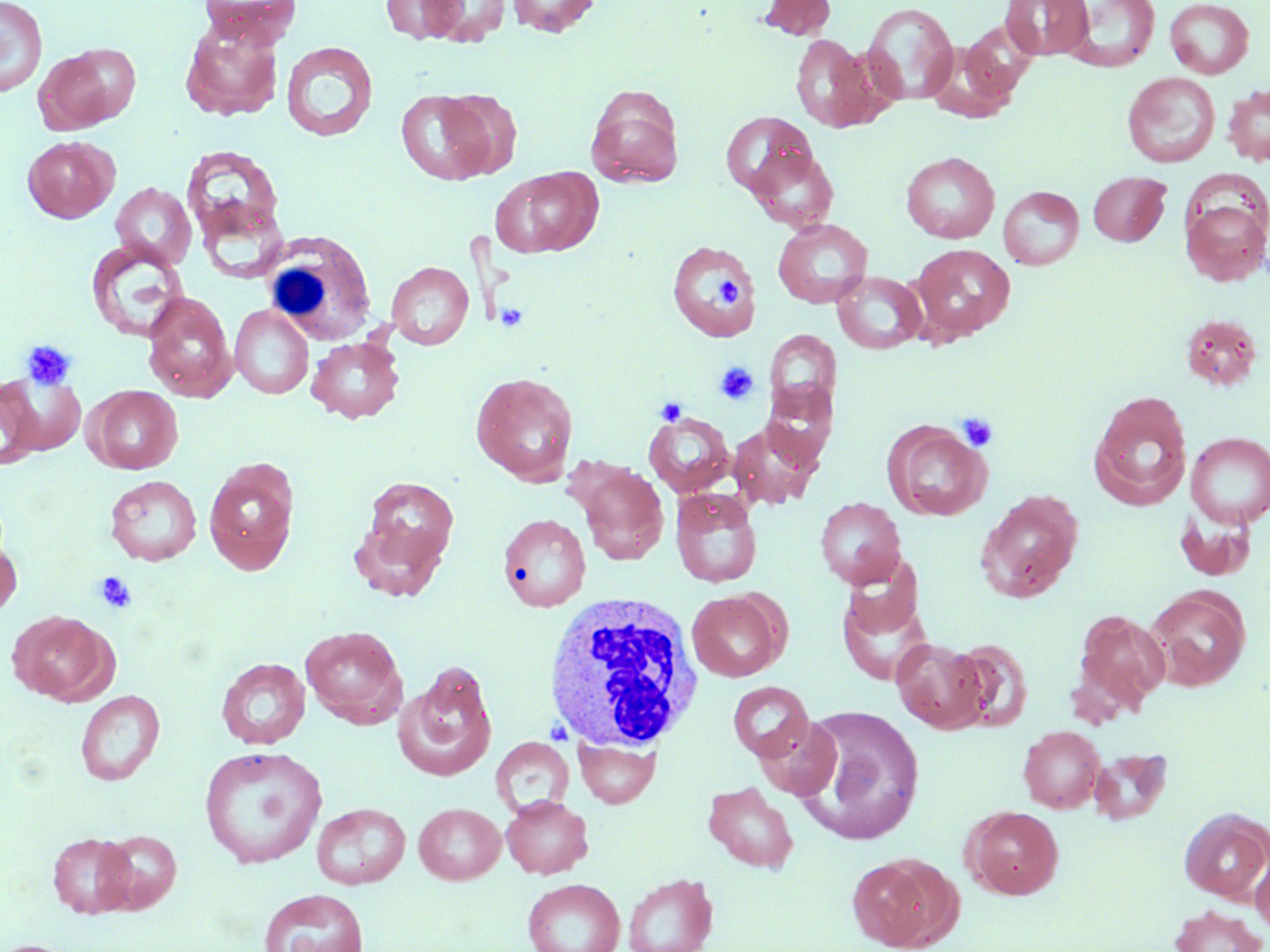
Approximate bounding boxes as [x1, y1, x2, y2] in pixels. Platelet locations: [714, 277, 742, 306], [495, 302, 529, 333], [21, 340, 76, 390], [714, 361, 759, 405], [655, 397, 687, 425], [957, 412, 998, 452], [94, 572, 137, 615]. White blood cell locations: [262, 229, 378, 352], [540, 592, 707, 752]. Uninfected red blood cell locations: [0, 0, 48, 98], [198, 0, 302, 47], [381, 0, 469, 44], [423, 0, 511, 45], [507, 0, 601, 37], [758, 0, 836, 40], [1001, 0, 1093, 60], [1061, 0, 1161, 72], [1165, 0, 1255, 79], [862, 3, 959, 106], [180, 19, 284, 121], [960, 24, 1038, 101], [790, 33, 880, 132], [280, 41, 378, 142], [35, 43, 140, 133], [1122, 71, 1220, 167], [1223, 83, 1270, 166], [585, 87, 685, 188], [395, 89, 495, 185], [438, 89, 522, 178], [720, 111, 816, 198], [22, 135, 118, 223], [181, 142, 288, 258], [747, 145, 838, 231], [900, 151, 999, 243], [492, 166, 603, 258], [1088, 171, 1170, 245], [110, 182, 196, 270], [998, 186, 1084, 270], [1180, 192, 1270, 287], [773, 218, 873, 308], [85, 238, 190, 343], [667, 241, 761, 341], [911, 244, 1015, 343], [386, 261, 474, 350], [832, 271, 927, 354], [141, 291, 238, 402], [230, 305, 314, 399], [764, 329, 841, 416], [306, 336, 405, 423], [1, 372, 86, 459], [470, 372, 579, 485], [1, 377, 44, 469], [761, 379, 838, 469], [85, 385, 183, 474], [1088, 392, 1192, 510], [644, 411, 735, 497], [728, 420, 822, 509], [884, 421, 992, 521], [1186, 432, 1270, 527], [203, 458, 299, 575], [572, 460, 670, 565], [105, 475, 202, 566], [361, 477, 459, 570], [670, 488, 762, 587], [975, 490, 1083, 603], [815, 497, 906, 589], [349, 513, 450, 602], [498, 513, 590, 612], [0, 530, 22, 620], [837, 584, 934, 686], [1144, 587, 1250, 690], [687, 590, 785, 681], [1073, 609, 1169, 715], [7, 610, 115, 705], [301, 625, 407, 727], [892, 637, 989, 734], [947, 638, 1033, 732], [216, 657, 311, 749], [394, 664, 497, 782], [727, 681, 814, 761], [75, 690, 165, 786], [791, 704, 924, 843], [754, 716, 843, 800], [1019, 725, 1106, 813], [574, 735, 660, 808], [490, 736, 574, 818], [199, 745, 327, 868], [1089, 747, 1172, 825], [702, 781, 799, 873], [502, 795, 593, 878], [312, 802, 411, 890], [413, 803, 506, 884], [964, 805, 1064, 900], [1179, 809, 1270, 901], [96, 829, 182, 913], [47, 831, 137, 918], [1251, 847, 1270, 936], [847, 852, 963, 951], [623, 873, 718, 952], [522, 878, 625, 952], [259, 888, 369, 952], [1168, 905, 1267, 952], [0, 939, 83, 952]. Slide-level diagnosis: no evidence of blood parasites. Image is 1270×952 pixels. Optical microscopy. Thin blood smear. May-Grünwald-Giemsa-stained preparation. One field of a larger specimen. Captured at 1000x magnification.